Assess this cell for malaria.
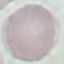
Uninfected.

capture = smartphone camera at the microscope eyepiece
stain = Giemsa
image type = cell patch, automatically extracted from a larger field of view and resized to 64 × 64 pixels
preparation = thin blood film